Assess the morphology of the red blood cells.
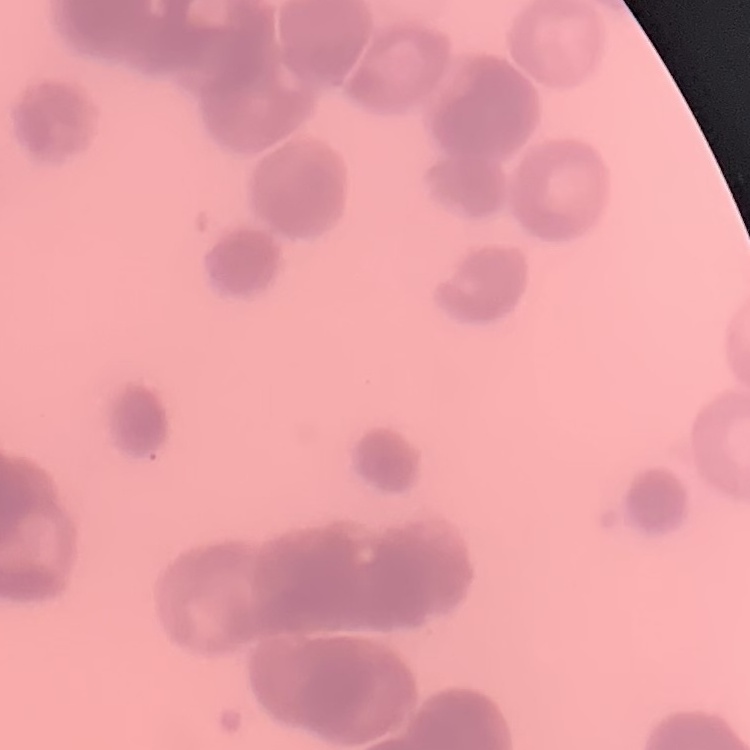

Rouleaux formation.

Summary:
  - Preparation: thin peripheral smear
  - Stain: Field's or Giemsa
  - Image type: square crop of a larger photomicrograph